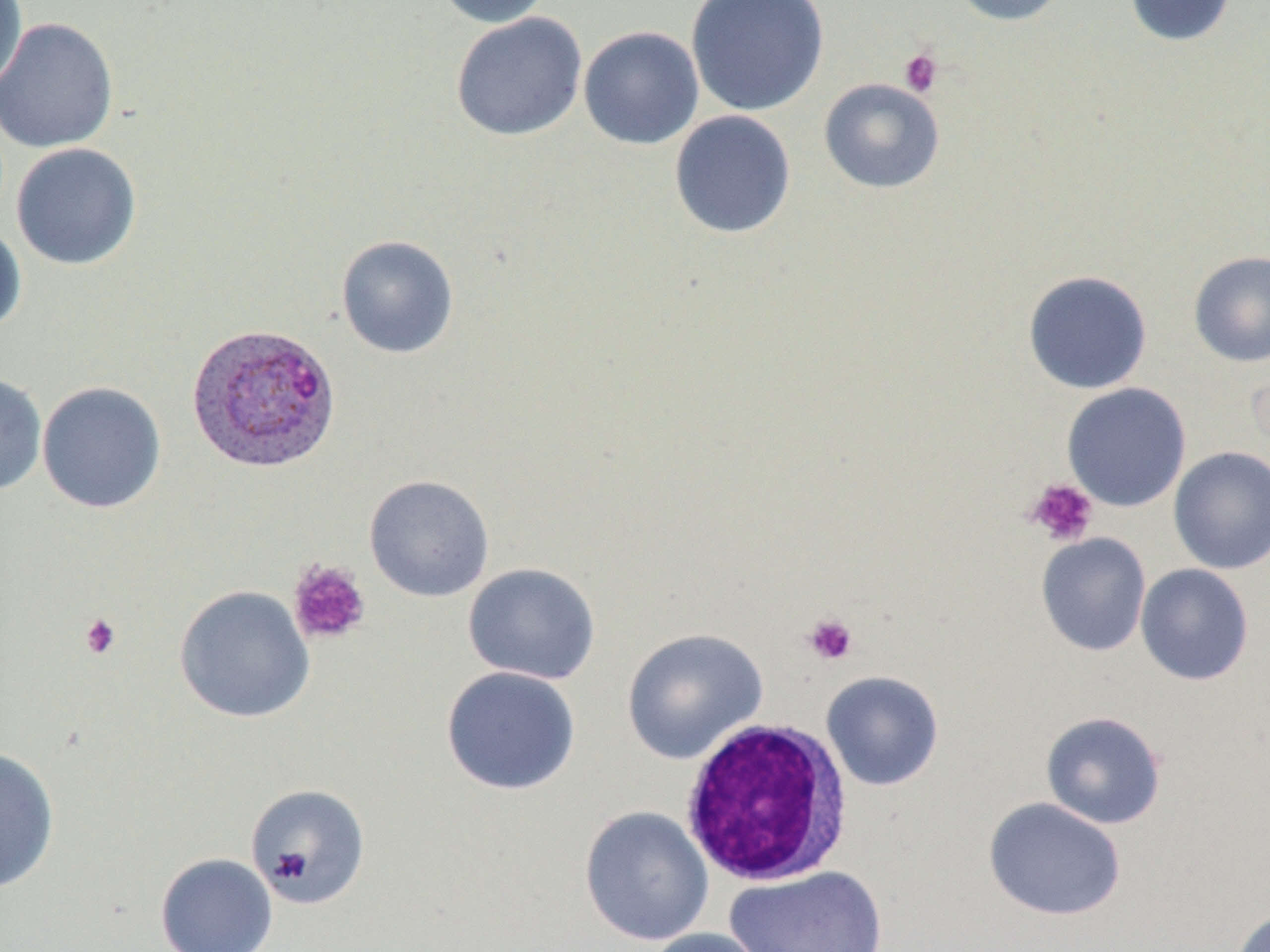

Summary:
  - Coordinate format: approximate bounding boxes as [x1, y1, x2, y2] in pixels
  - Plasmodium ovale-infected red blood cell locations: [185, 321, 342, 473]
  - Platelet locations: [898, 48, 944, 97], [1025, 478, 1099, 547], [287, 559, 371, 645], [80, 613, 122, 659], [802, 613, 858, 666]
  - White blood cell locations: [679, 717, 855, 887]
  - Uninfected red blood cell locations: [0, 0, 29, 94], [433, 0, 553, 28], [686, 0, 829, 117], [949, 0, 1070, 26], [1123, 0, 1236, 47], [450, 11, 587, 141], [0, 17, 119, 153], [578, 26, 704, 150], [818, 78, 945, 194], [669, 110, 797, 239], [10, 142, 143, 271], [0, 221, 27, 337], [335, 235, 459, 359], [1188, 250, 1270, 368], [1022, 269, 1153, 394], [0, 371, 48, 497], [36, 380, 167, 513], [1061, 382, 1191, 512], [1168, 446, 1270, 575], [363, 475, 495, 602], [1035, 532, 1151, 656], [462, 562, 601, 685], [1135, 563, 1254, 685], [174, 585, 315, 724], [621, 628, 768, 764], [440, 666, 581, 796], [821, 670, 944, 791], [1040, 711, 1167, 829], [0, 746, 60, 894], [246, 783, 371, 909], [983, 797, 1126, 922], [579, 806, 714, 946], [156, 852, 278, 952], [726, 865, 887, 952], [1229, 908, 1270, 952], [643, 927, 771, 952]
  - Slide-level diagnosis: Plasmodium ovale
  - Modality: light microscopy
  - Preparation: thin blood film
  - Stain: May-Grünwald-Giemsa
  - Magnification: 1000x
  - Field of view: one of a larger specimen
  - Image size: 1270×952 pixels